Name the blood parasite species.
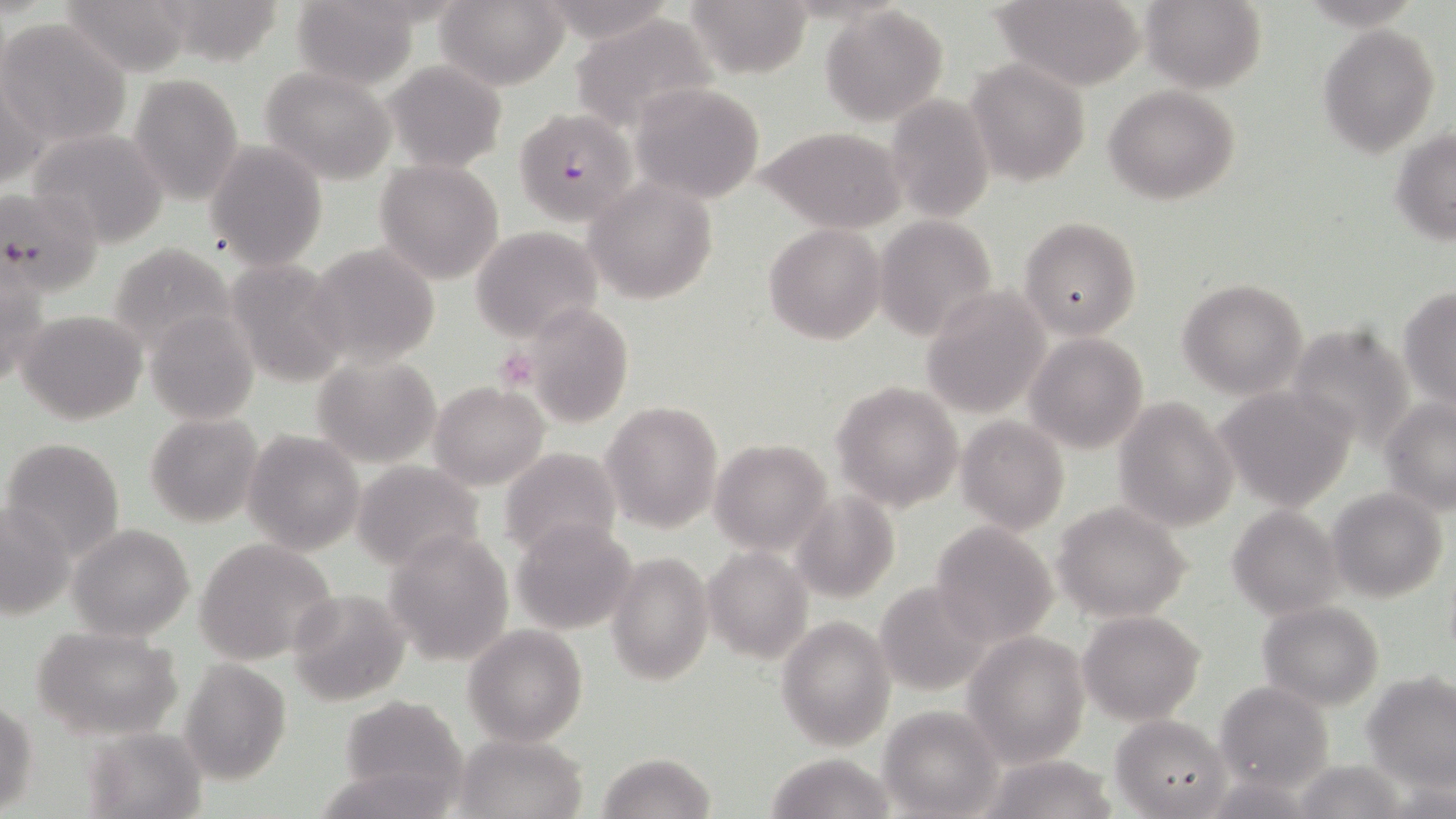

Plasmodium falciparum.

Approximate bounding boxes as (x1,y1)-(x2,y2) corner pairs in pixels. Platelet locations: (494,347)-(538,390). Uninfected red blood cell locations: (60,0)-(192,75), (150,0)-(287,67), (288,0)-(424,89), (434,0)-(570,90), (682,0)-(813,75), (989,0)-(1147,89), (1141,0)-(1267,93), (819,5)-(949,127), (571,13)-(718,133), (1,18)-(132,149), (1317,22)-(1440,158), (385,60)-(508,172), (967,60)-(1089,185), (259,66)-(397,184), (1,68)-(46,194), (129,73)-(245,207), (629,81)-(766,204), (1104,84)-(1242,204), (887,97)-(996,222), (757,126)-(907,231), (25,127)-(172,247), (1391,127)-(1456,245), (207,142)-(327,270), (374,158)-(505,285), (584,179)-(718,304), (0,186)-(104,296), (874,216)-(995,339), (1019,217)-(1140,339), (763,223)-(887,346), (471,225)-(605,343), (306,242)-(441,368), (108,243)-(236,352), (223,258)-(350,385), (1,259)-(46,391), (1178,278)-(1308,399), (921,286)-(1052,417), (1399,286)-(1456,409), (517,299)-(636,429), (145,308)-(261,426), (17,311)-(148,426), (1283,322)-(1420,452), (1024,333)-(1149,454), (311,353)-(442,467), (428,381)-(549,490), (831,381)-(964,512), (1214,384)-(1359,511), (1112,396)-(1238,531), (1380,397)-(1456,513), (602,400)-(723,534), (145,413)-(264,528), (955,415)-(1070,534), (242,429)-(365,555), (1,435)-(125,562), (709,438)-(834,555), (498,447)-(623,562), (351,461)-(486,571), (1327,487)-(1448,604), (792,489)-(899,602), (1052,500)-(1194,622), (0,502)-(74,621), (1227,505)-(1344,620), (510,520)-(637,634), (930,521)-(1058,643), (68,523)-(195,641), (382,529)-(515,666), (194,537)-(340,665), (703,547)-(812,663), (607,550)-(715,687), (874,581)-(994,696), (287,588)-(408,706), (1257,600)-(1384,710), (1077,609)-(1206,725), (775,615)-(897,751), (30,624)-(185,741), (463,625)-(588,746), (961,630)-(1092,767), (179,658)-(292,784), (1363,673)-(1456,792), (1214,681)-(1334,797), (336,695)-(470,808), (0,702)-(39,816), (877,706)-(1002,818), (1109,713)-(1231,817), (82,725)-(206,817), (453,732)-(589,819), (597,751)-(716,819), (763,753)-(895,818), (978,753)-(1121,819), (1290,759)-(1415,818). Plasmodium falciparum-infected red blood cell locations: (511,107)-(636,225). Light microscopy. Image is 1456×819 pixels. May-Grünwald-Giemsa-stained preparation. One field of a larger specimen. Captured at 1000x magnification. Thin blood smear.